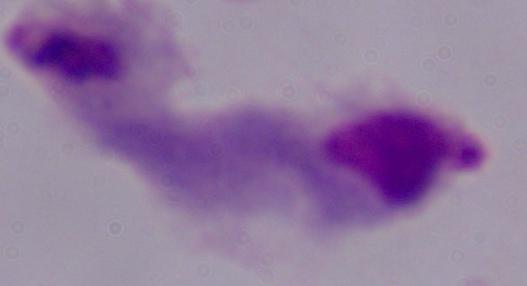
magnification = 1000x
identification = trichomonad
modality = photomicrograph